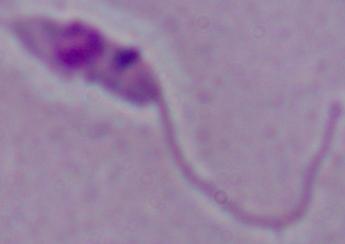

Summary:
  - Magnification: 1000x
  - Identification: Leishmania
  - Modality: micrograph